Assess the morphology of the red blood cells.
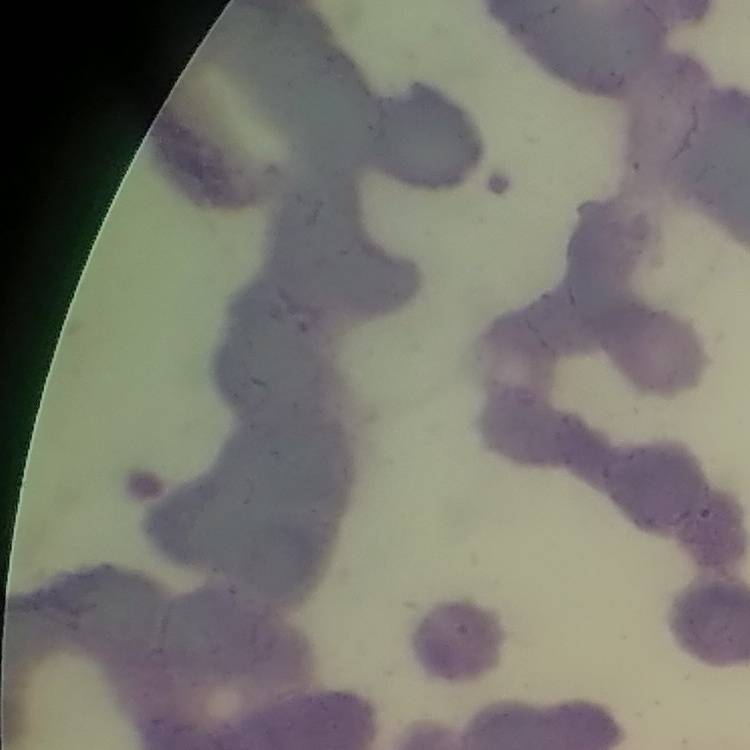
They show rouleaux formation.

stain = Field's or Giemsa
image type = one tile cut from a larger photomicrograph
preparation = thin blood film